Locate every blood parasite and identify its species.
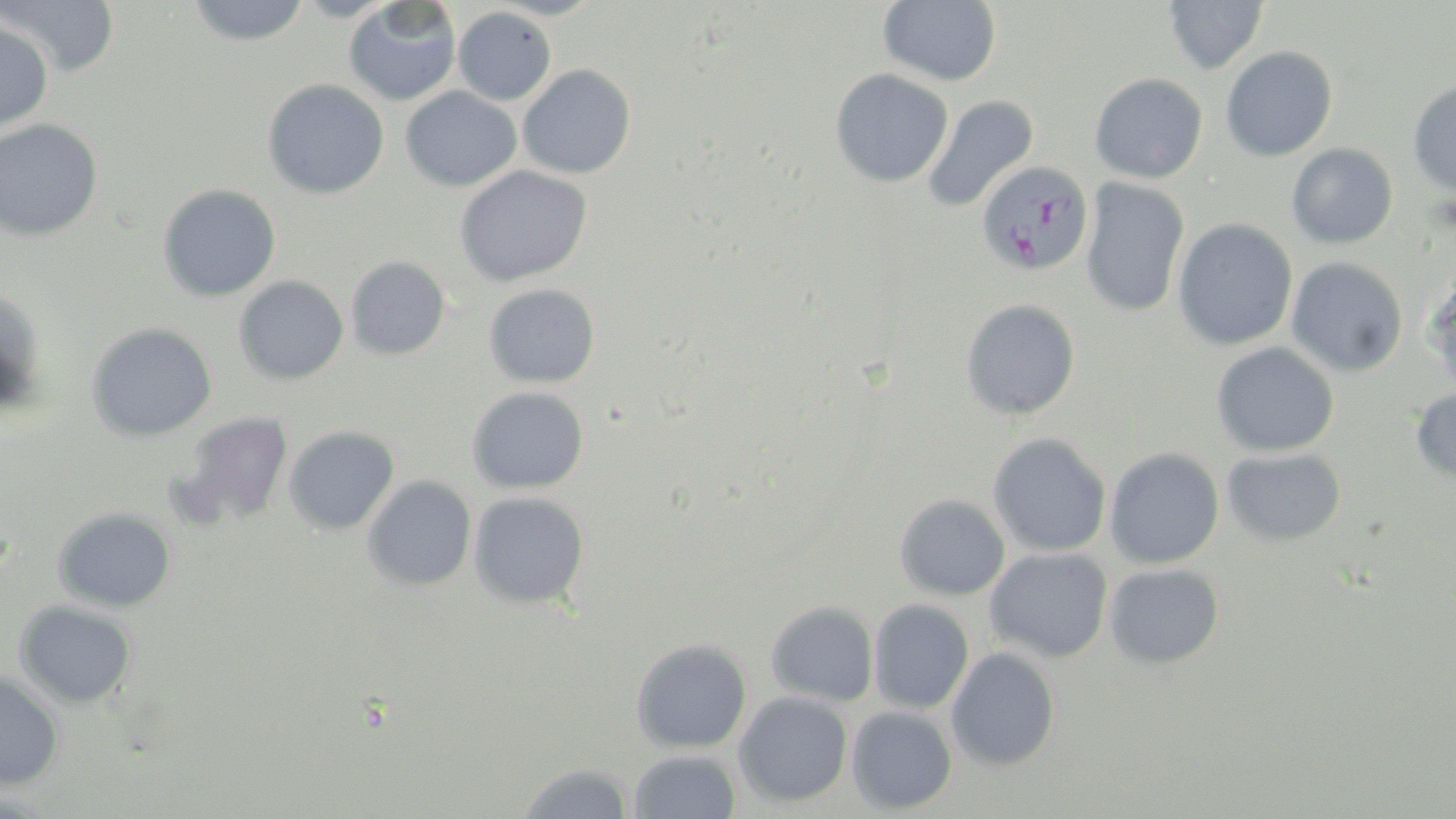
Approximate bounding boxes as named x1/y1/x2/y2 corners in pixels.
Plasmodium falciparum-infected red blood cells: (x1=976, y1=159, x2=1093, y2=277).
No Plasmodium ovale, Plasmodium malariae, Plasmodium vivax, Babesia divergens, or Trypanosoma brucei observed.

Uninfected red blood cell locations: (x1=3, y1=0, x2=120, y2=76), (x1=878, y1=0, x2=1001, y2=85), (x1=1164, y1=0, x2=1268, y2=74), (x1=187, y1=1, x2=311, y2=46), (x1=343, y1=2, x2=461, y2=106), (x1=453, y1=7, x2=556, y2=105), (x1=0, y1=21, x2=53, y2=132), (x1=1220, y1=46, x2=1338, y2=161), (x1=518, y1=65, x2=636, y2=179), (x1=830, y1=68, x2=953, y2=188), (x1=1089, y1=72, x2=1208, y2=183), (x1=262, y1=78, x2=389, y2=199), (x1=1407, y1=78, x2=1456, y2=196), (x1=401, y1=86, x2=521, y2=191), (x1=921, y1=95, x2=1039, y2=214), (x1=0, y1=119, x2=103, y2=241), (x1=1286, y1=143, x2=1398, y2=248), (x1=455, y1=165, x2=592, y2=286), (x1=1080, y1=178, x2=1190, y2=317), (x1=157, y1=184, x2=281, y2=302), (x1=1173, y1=218, x2=1298, y2=350), (x1=345, y1=256, x2=450, y2=360), (x1=1287, y1=257, x2=1408, y2=377), (x1=1423, y1=272, x2=1456, y2=395), (x1=234, y1=276, x2=348, y2=384), (x1=484, y1=284, x2=600, y2=388), (x1=0, y1=288, x2=47, y2=412), (x1=961, y1=299, x2=1081, y2=420), (x1=86, y1=323, x2=216, y2=442), (x1=1212, y1=342, x2=1339, y2=457), (x1=467, y1=386, x2=589, y2=494), (x1=1409, y1=387, x2=1456, y2=485), (x1=176, y1=412, x2=294, y2=527), (x1=284, y1=426, x2=399, y2=535), (x1=988, y1=433, x2=1112, y2=557), (x1=1105, y1=447, x2=1225, y2=568), (x1=1222, y1=448, x2=1346, y2=546), (x1=362, y1=475, x2=477, y2=591), (x1=469, y1=491, x2=590, y2=609), (x1=895, y1=494, x2=1010, y2=600), (x1=53, y1=507, x2=176, y2=612), (x1=986, y1=547, x2=1113, y2=662), (x1=1105, y1=564, x2=1224, y2=669), (x1=868, y1=599, x2=974, y2=713), (x1=15, y1=600, x2=136, y2=708), (x1=766, y1=600, x2=879, y2=706), (x1=631, y1=638, x2=752, y2=753), (x1=946, y1=647, x2=1060, y2=771), (x1=0, y1=672, x2=64, y2=791), (x1=734, y1=691, x2=853, y2=807), (x1=847, y1=706, x2=958, y2=814), (x1=628, y1=749, x2=742, y2=819), (x1=517, y1=762, x2=635, y2=819). Slide-level diagnosis: Plasmodium falciparum. Single field of view. Image is 1456×819 pixels. Light microscopy. Thin blood film. 1000x magnification. May-Grünwald-Giemsa stain.